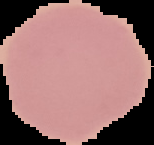

Summary:
  - Preparation: thin blood smear
  - Image type: cell region segmented out of the field of view; surrounding area masked to black
  - Image size: 154×145 pixels
  - Result: no malaria parasites seen